Locate and identify every blood parasite.
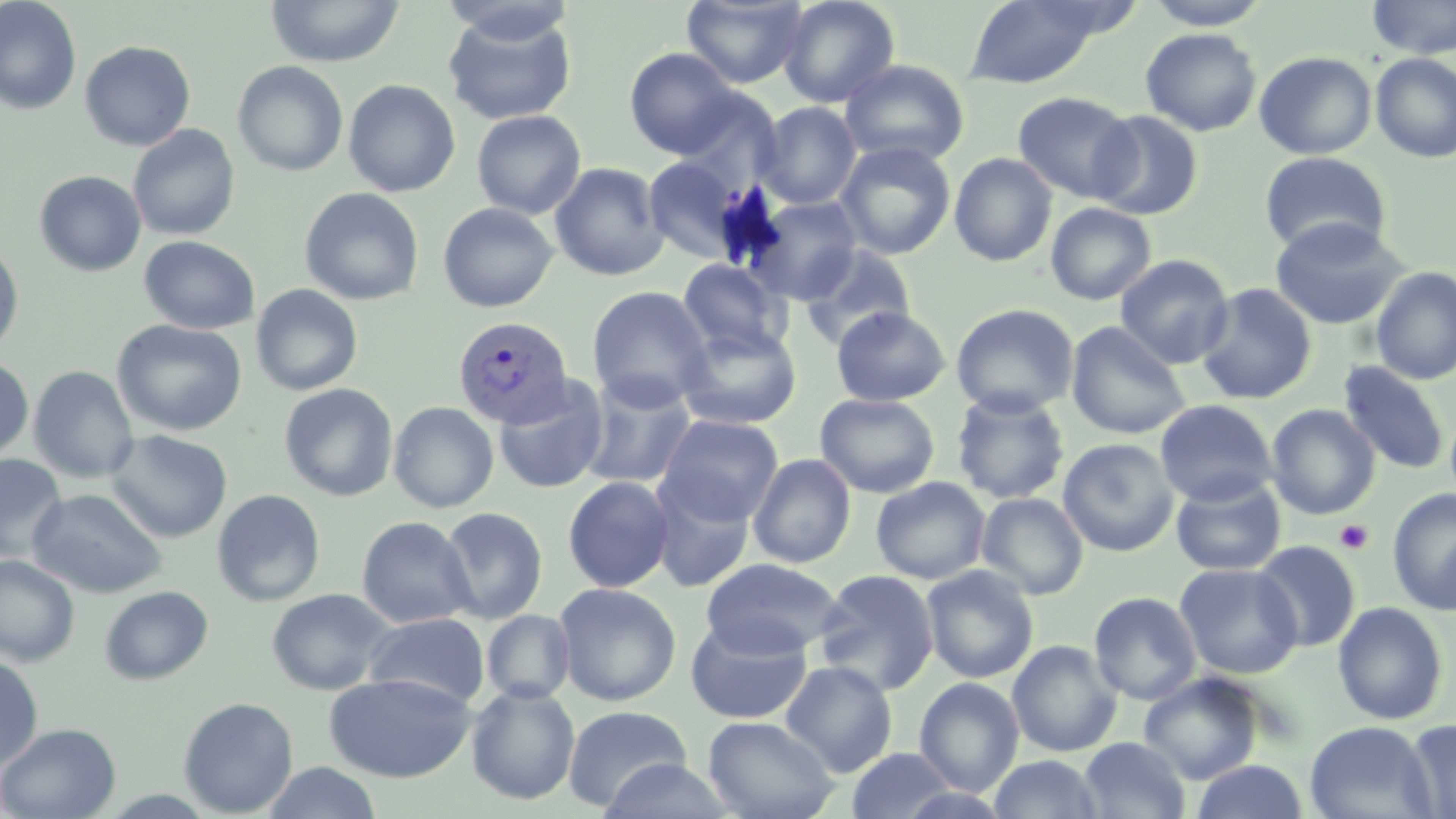
Approximate bounding boxes as named x1/y1/x2/y2 corners in pixels.
Plasmodium vivax-infected red blood cells: (x1=452, y1=316, x2=574, y2=428).
No Plasmodium falciparum, Plasmodium ovale, Plasmodium malariae, Babesia divergens, or Trypanosoma brucei observed.

Uninfected red blood cell locations: (x1=0, y1=0, x2=82, y2=115), (x1=439, y1=0, x2=578, y2=45), (x1=681, y1=0, x2=809, y2=89), (x1=777, y1=0, x2=900, y2=108), (x1=963, y1=0, x2=1110, y2=89), (x1=1143, y1=0, x2=1274, y2=30), (x1=1366, y1=0, x2=1456, y2=59), (x1=265, y1=1, x2=405, y2=68), (x1=443, y1=11, x2=577, y2=125), (x1=1140, y1=28, x2=1263, y2=137), (x1=80, y1=40, x2=195, y2=151), (x1=624, y1=48, x2=740, y2=158), (x1=1253, y1=51, x2=1378, y2=160), (x1=1370, y1=53, x2=1456, y2=163), (x1=839, y1=59, x2=971, y2=167), (x1=232, y1=60, x2=349, y2=176), (x1=342, y1=79, x2=461, y2=197), (x1=674, y1=88, x2=785, y2=191), (x1=1012, y1=91, x2=1139, y2=203), (x1=756, y1=102, x2=862, y2=209), (x1=471, y1=110, x2=586, y2=219), (x1=1088, y1=110, x2=1205, y2=220), (x1=127, y1=124, x2=240, y2=241), (x1=834, y1=141, x2=957, y2=260), (x1=1259, y1=151, x2=1391, y2=256), (x1=949, y1=152, x2=1057, y2=266), (x1=642, y1=156, x2=749, y2=263), (x1=549, y1=162, x2=669, y2=282), (x1=34, y1=171, x2=146, y2=276), (x1=300, y1=187, x2=424, y2=306), (x1=746, y1=196, x2=864, y2=305), (x1=437, y1=202, x2=558, y2=313), (x1=1045, y1=202, x2=1157, y2=306), (x1=1269, y1=217, x2=1409, y2=330), (x1=139, y1=235, x2=260, y2=334), (x1=0, y1=243, x2=25, y2=360), (x1=799, y1=243, x2=917, y2=350), (x1=1115, y1=254, x2=1234, y2=369), (x1=677, y1=258, x2=792, y2=358), (x1=1371, y1=266, x2=1456, y2=385), (x1=1195, y1=283, x2=1317, y2=405), (x1=250, y1=284, x2=363, y2=396), (x1=586, y1=286, x2=713, y2=411), (x1=951, y1=303, x2=1080, y2=418), (x1=831, y1=306, x2=950, y2=407), (x1=112, y1=319, x2=247, y2=436), (x1=1066, y1=321, x2=1192, y2=440), (x1=674, y1=322, x2=802, y2=430), (x1=0, y1=356, x2=34, y2=464), (x1=1338, y1=361, x2=1451, y2=476), (x1=28, y1=366, x2=139, y2=483), (x1=579, y1=374, x2=697, y2=490), (x1=493, y1=377, x2=610, y2=494), (x1=279, y1=383, x2=399, y2=501), (x1=951, y1=390, x2=1070, y2=505), (x1=815, y1=393, x2=939, y2=498), (x1=1154, y1=399, x2=1278, y2=507), (x1=388, y1=401, x2=499, y2=514), (x1=1266, y1=404, x2=1380, y2=520), (x1=656, y1=414, x2=784, y2=526), (x1=104, y1=430, x2=232, y2=543), (x1=1057, y1=438, x2=1179, y2=556), (x1=0, y1=453, x2=68, y2=564), (x1=748, y1=453, x2=856, y2=568), (x1=649, y1=475, x2=755, y2=593), (x1=1170, y1=475, x2=1287, y2=577), (x1=562, y1=476, x2=675, y2=593), (x1=871, y1=476, x2=991, y2=585), (x1=27, y1=488, x2=167, y2=598), (x1=1387, y1=488, x2=1456, y2=616), (x1=211, y1=489, x2=326, y2=607), (x1=976, y1=492, x2=1089, y2=600), (x1=438, y1=506, x2=548, y2=624), (x1=356, y1=516, x2=476, y2=628), (x1=1251, y1=540, x2=1362, y2=653), (x1=0, y1=555, x2=80, y2=667), (x1=701, y1=558, x2=846, y2=658), (x1=1174, y1=563, x2=1303, y2=680), (x1=921, y1=565, x2=1039, y2=684), (x1=813, y1=568, x2=940, y2=696), (x1=553, y1=582, x2=682, y2=706), (x1=99, y1=585, x2=214, y2=685), (x1=266, y1=588, x2=396, y2=695), (x1=1089, y1=591, x2=1202, y2=705), (x1=1332, y1=601, x2=1449, y2=725), (x1=481, y1=610, x2=576, y2=704), (x1=362, y1=612, x2=490, y2=710), (x1=684, y1=615, x2=813, y2=725), (x1=1007, y1=639, x2=1123, y2=757), (x1=0, y1=655, x2=44, y2=771), (x1=780, y1=661, x2=898, y2=776), (x1=323, y1=671, x2=476, y2=783), (x1=1138, y1=672, x2=1265, y2=784), (x1=779, y1=673, x2=1024, y2=782), (x1=914, y1=678, x2=1024, y2=796), (x1=466, y1=684, x2=580, y2=805), (x1=178, y1=697, x2=299, y2=817), (x1=562, y1=704, x2=692, y2=813), (x1=702, y1=715, x2=840, y2=819), (x1=1401, y1=718, x2=1456, y2=819), (x1=1305, y1=721, x2=1436, y2=819), (x1=0, y1=722, x2=121, y2=818), (x1=1078, y1=737, x2=1191, y2=819), (x1=845, y1=747, x2=961, y2=819), (x1=1079, y1=749, x2=1306, y2=817), (x1=987, y1=755, x2=1105, y2=818), (x1=596, y1=758, x2=737, y2=818), (x1=1191, y1=759, x2=1308, y2=818), (x1=261, y1=761, x2=384, y2=819). Platelet locations: (x1=1335, y1=520, x2=1374, y2=553). Slide-level diagnosis: Plasmodium vivax. Optical microscopy. Single field of view. Thin blood smear. Captured at 1000x magnification. May-Grünwald-Giemsa stain. Image is 1456×819 pixels.